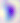

Micrograph. 400x magnification. Toxoplasma gondii is shown.